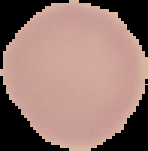

Segmented cell region on a black background. Image is 148×151 pixels. Result: negative for Plasmodium parasites. From a thin blood film.